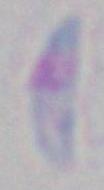

Summary:
  - Magnification: 1000x
  - Identification: Toxoplasma gondii
  - Modality: micrograph